Describe the morphology of the erythrocytes.
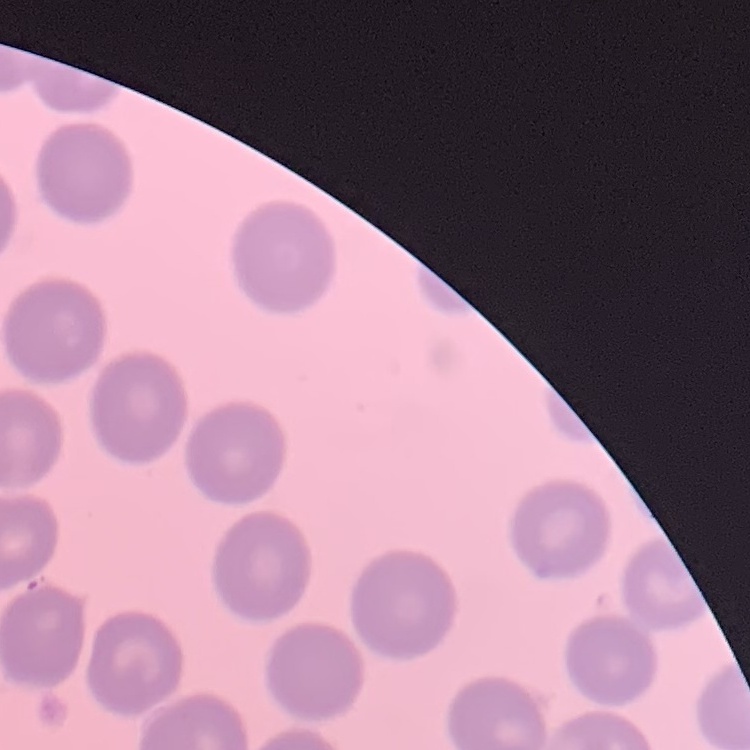

No rouleaux formation.

image type = square crop of a larger photomicrograph
stain = Field's or Giemsa
preparation = thin blood film